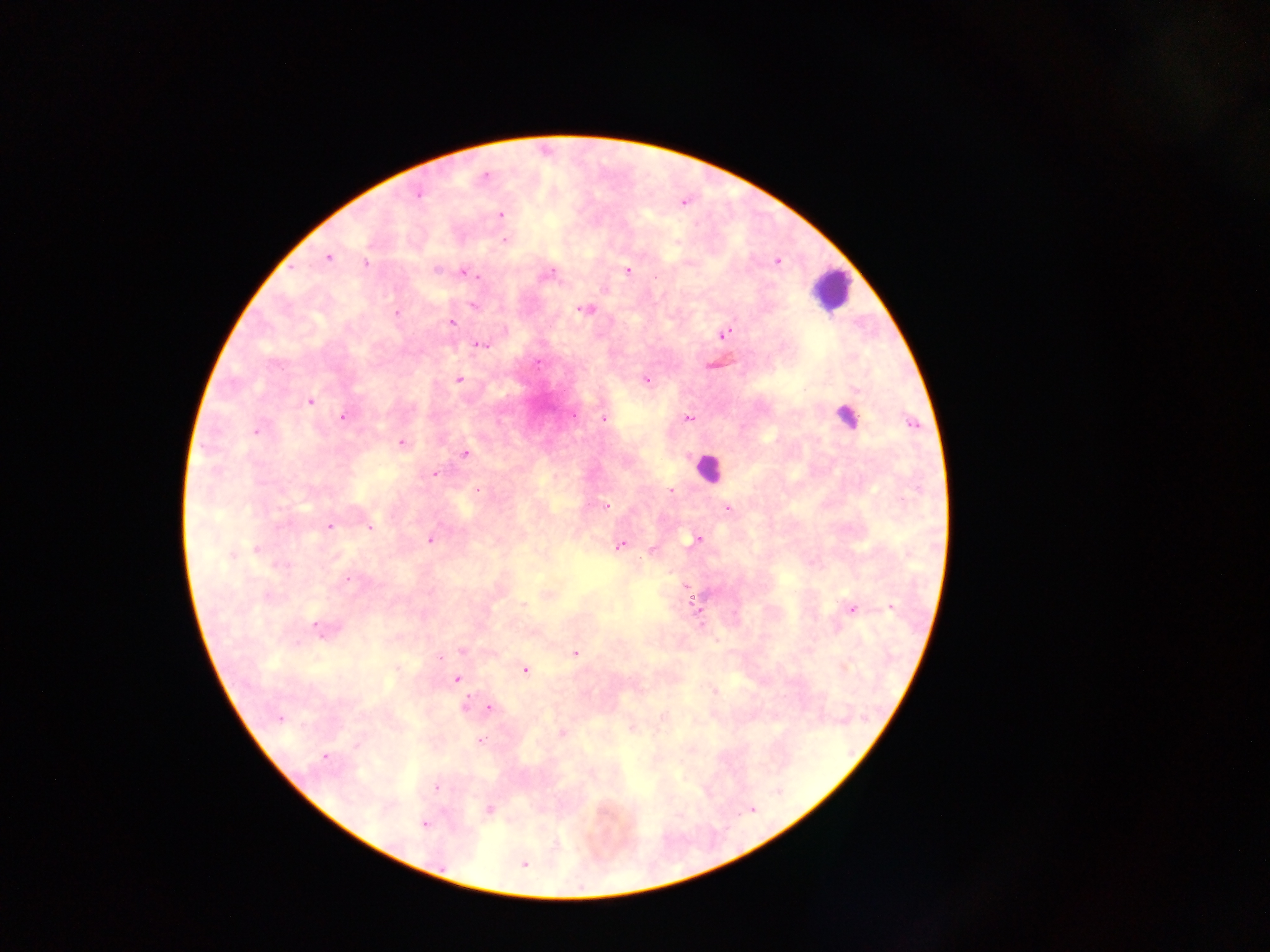
Approximate centers as x y in pixels. Plasmodium parasite locations: 485 175; 418 195; 684 203; 500 214; 506 240; 328 257; 777 261; 366 263; 436 270; 628 271; 466 274; 549 274; 474 276; 474 305; 586 309; 397 313; 451 323; 724 334; 481 345; 538 363; 459 379; 645 380; 856 389; 309 401; 574 415; 343 417; 603 419; 689 419; 911 422; 256 431; 401 443; 465 453; 435 474; 477 489; 671 490; 606 506; 728 508; 330 526; 370 527; 695 540; 430 541; 620 546; 256 548; 652 551; 231 555; 281 565; 348 579; 686 586; 267 595; 523 604; 891 607; 853 609; 317 627; 461 651; 575 653; 439 657; 398 668; 525 670; 456 678; 714 691; 465 705; 490 708; 280 718; 631 729; 561 733; 480 740; 356 746; 325 757; 437 787; 489 810; 424 824; 523 864. Leukocyte locations: 830 290; 842 414; 709 468. Mobile-phone photograph taken through the microscope. Thick blood smear. Single field of view. Sample from Ghana. Image is 1270×952 pixels.